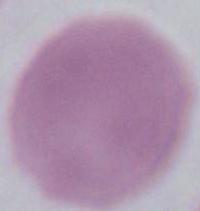
Summary:
  - Identification: red blood cell
  - Magnification: 1000x
  - Modality: micrograph